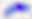

Micrograph. Captured at 400x magnification. Toxoplasma gondii is shown.